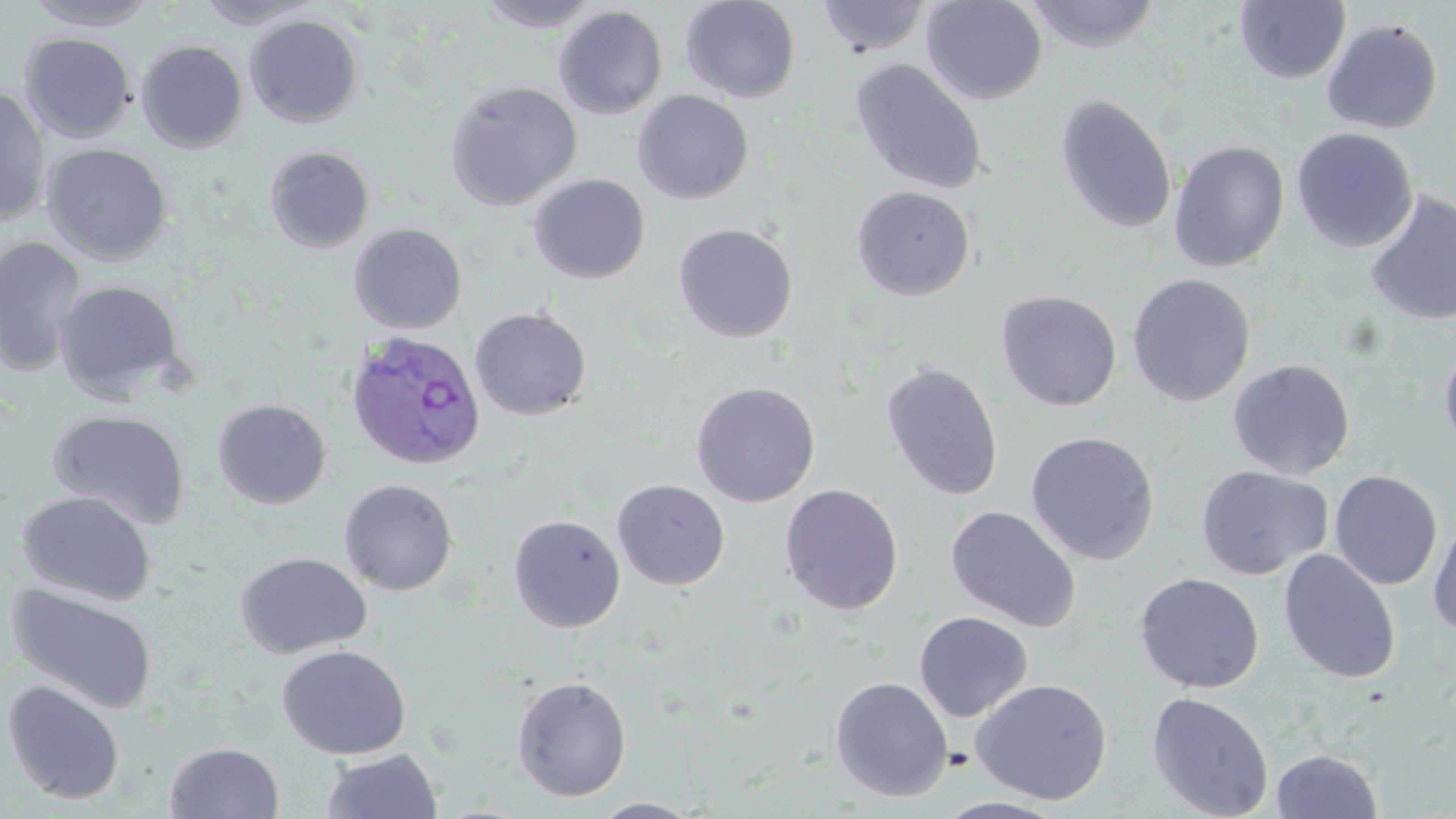

Summary:
  - Coordinate format: approximate bounding boxes as (x1,y1)-(x2,y2) corner pairs in pixels
  - Uninfected red blood cell locations: (23,0)-(160,30), (194,0)-(320,29), (476,0)-(607,32), (681,0)-(801,103), (817,0)-(931,56), (922,0)-(1048,105), (1025,0)-(1162,52), (1235,1)-(1351,85), (554,6)-(668,119), (245,15)-(364,128), (1321,18)-(1443,135), (20,33)-(136,142), (136,40)-(248,153), (851,59)-(988,195), (444,80)-(583,211), (0,86)-(52,227), (633,90)-(754,204), (1056,94)-(1177,234), (1292,128)-(1418,252), (1169,140)-(1290,271), (42,143)-(173,264), (265,146)-(375,253), (529,174)-(651,284), (851,186)-(975,300), (1364,191)-(1456,327), (349,223)-(467,334), (673,223)-(798,343), (0,236)-(86,377), (1127,273)-(1256,407), (55,280)-(186,402), (996,290)-(1122,411), (469,307)-(593,421), (1439,342)-(1456,457), (1227,359)-(1355,480), (879,362)-(1004,502), (691,381)-(820,507), (212,399)-(332,509), (47,408)-(192,529), (1025,430)-(1160,565), (1195,465)-(1334,580), (1329,469)-(1443,590), (339,479)-(459,596), (612,479)-(730,590), (779,484)-(904,615), (18,491)-(156,605), (945,505)-(1081,632), (1427,512)-(1456,637), (508,514)-(625,632), (1278,548)-(1401,684), (235,551)-(371,658), (1134,571)-(1265,693), (8,583)-(158,713), (914,611)-(1033,722), (277,645)-(411,759), (511,675)-(632,801), (830,676)-(953,802), (970,677)-(1113,805), (2,678)-(125,805), (1147,691)-(1274,819), (164,741)-(285,819), (321,749)-(442,819), (1271,749)-(1383,818), (931,795)-(1072,818), (588,797)-(706,818)
  - Plasmodium ovale-infected red blood cell locations: (345,330)-(487,471)
  - Slide-level diagnosis: Plasmodium ovale
  - Modality: optical microscopy
  - Image size: 1456×819 pixels
  - Field of view: single
  - Preparation: thin blood smear
  - Stain: May-Grünwald-Giemsa
  - Magnification: 1000x